Report the malaria status of this cell.
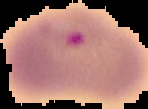

It is parasitized.

Summary:
  - Preparation: thin blood film
  - Image type: cell region segmented out of the field of view; surrounding area masked to black
  - Image size: 148×109 pixels